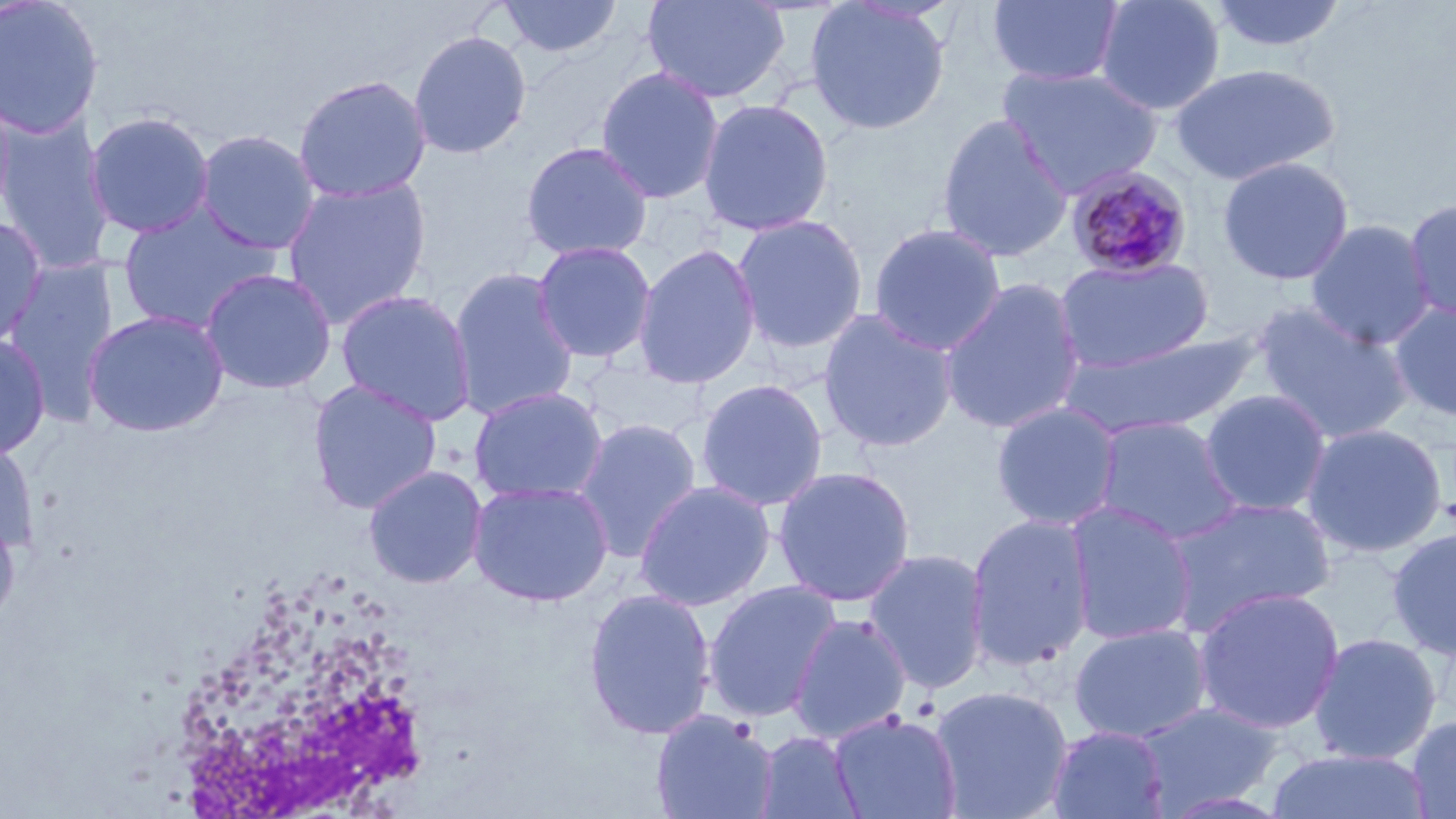

Summary:
  - Coordinate format: approximate bounding boxes as [x1, y1, x2, y2] in pixels
  - Uninfected red blood cell locations (subset): [496, 0, 623, 59], [642, 0, 790, 104], [986, 0, 1125, 86], [1093, 0, 1227, 116], [1208, 0, 1348, 54], [0, 1, 105, 140], [804, 1, 951, 135], [408, 30, 532, 160], [1168, 62, 1341, 185], [595, 66, 724, 204], [292, 74, 432, 203], [0, 88, 17, 223], [697, 98, 834, 236], [84, 111, 215, 239], [0, 113, 115, 273], [935, 114, 1074, 263], [194, 129, 322, 255], [519, 141, 654, 261], [1218, 156, 1355, 286], [281, 177, 432, 327], [1403, 197, 1456, 324], [118, 202, 280, 334], [730, 214, 869, 353], [0, 217, 47, 350], [1305, 219, 1435, 349], [868, 222, 1007, 355], [532, 241, 657, 363], [633, 243, 761, 389], [1054, 256, 1213, 373], [2, 258, 120, 423], [447, 266, 579, 420], [199, 268, 337, 395], [940, 278, 1086, 436], [335, 288, 477, 426], [1388, 300, 1455, 421], [1253, 303, 1415, 444], [818, 308, 959, 453], [83, 310, 229, 437], [1060, 331, 1263, 438], [0, 334, 51, 460], [577, 358, 707, 439], [695, 378, 829, 511], [307, 379, 442, 515], [469, 386, 609, 504], [1200, 389, 1332, 516], [990, 402, 1122, 531], [1092, 416, 1245, 546], [573, 417, 703, 562], [1301, 422, 1448, 557], [0, 439, 39, 556], [362, 464, 488, 589], [772, 465, 917, 607], [633, 479, 776, 611], [469, 480, 614, 606], [1163, 496, 1336, 634], [1064, 501, 1198, 645], [0, 509, 21, 630], [965, 513, 1096, 673], [1386, 526, 1456, 660], [862, 548, 992, 694], [702, 579, 843, 722], [1192, 587, 1344, 734], [582, 588, 717, 741], [788, 613, 912, 744], [1068, 622, 1212, 743], [1308, 633, 1442, 764], [931, 684, 1074, 818], [1134, 701, 1284, 814], [650, 708, 779, 819], [829, 710, 962, 819], [1405, 715, 1456, 818], [1046, 725, 1170, 819], [754, 730, 863, 819], [1265, 748, 1433, 819]
  - White blood cell locations: [181, 568, 428, 819]
  - Plasmodium malariae-infected red blood cell locations (subset): [1065, 164, 1194, 280]
  - Slide-level diagnosis: Plasmodium malariae
  - Modality: light microscopy
  - Field of view: single
  - Preparation: thin blood film
  - Image size: 1456×819 pixels
  - Stain: May-Grünwald-Giemsa
  - Magnification: 1000x